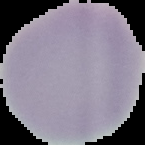

Summary:
  - Result: no malaria parasites seen
  - Image size: 145×145 pixels
  - Preparation: thin blood film
  - Image type: cell region segmented out of the field of view; surrounding area masked to black